Assess for Plasmodium parasites.
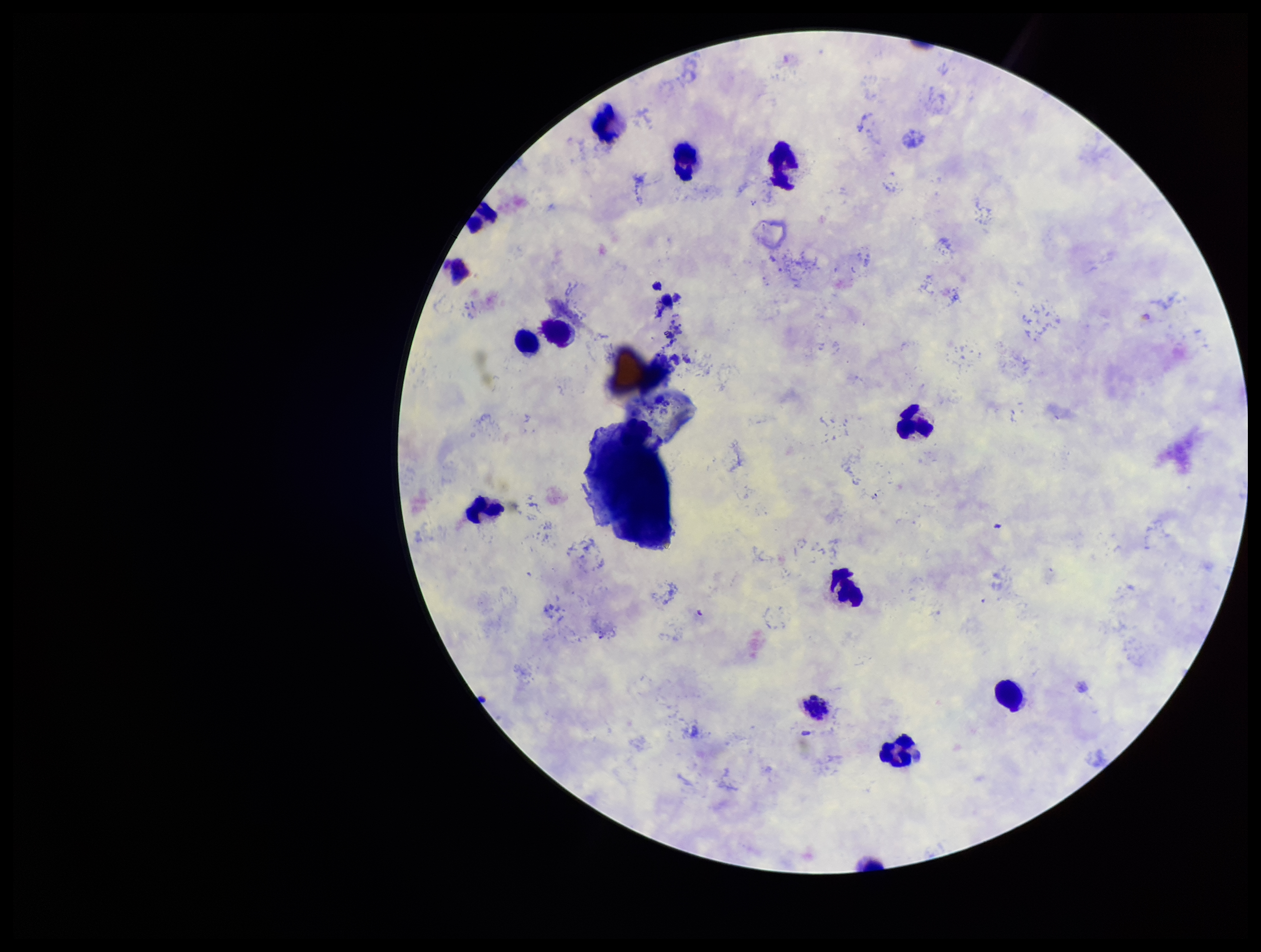

None seen.

capture = smartphone photograph through the microscope eyepiece
parasite count = 0
leukocyte count = 14
patient malaria status = infected
species reported for this patient = Plasmodium vivax
preparation = thick blood smear
image size = 1261×952 pixels
stain = Giemsa
field of view = one from this slide